Give the position of every Plasmodium parasite visible.
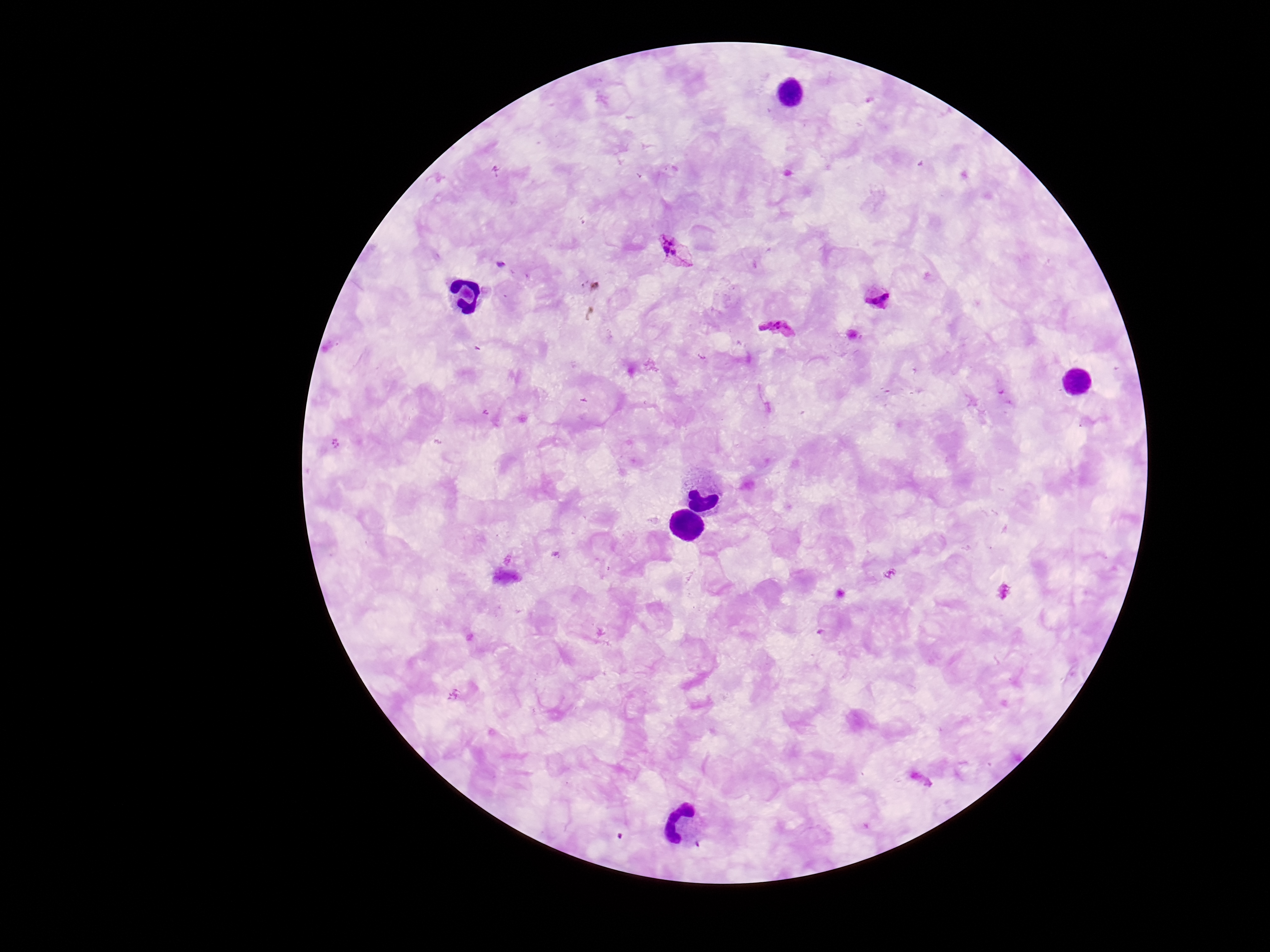

Approximate centers as {x, y} in pixels.
Plasmodium parasites: {674, 253}, {878, 295}, {778, 327}.

Summary:
  - Field of view: one from this slide
  - Image size: 1270×952 pixels
  - Capture: smartphone camera through the microscope eyepiece
  - Magnification: 100x
  - Preparation: thick blood film
  - Patient malaria status: infected
  - Stain: Giemsa